Comment on the morphology of the red blood cells.
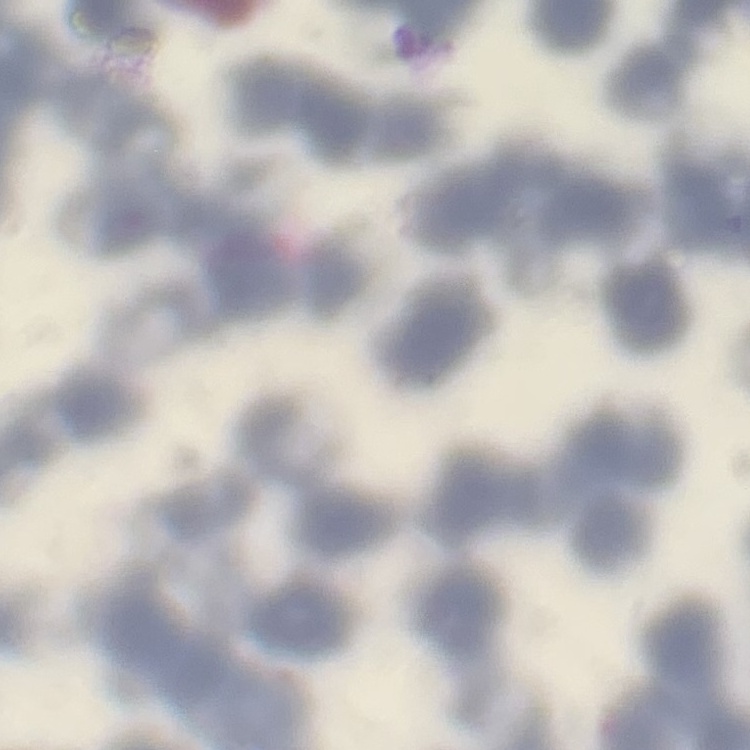

Rouleaux formation.

Summary:
  - Image type: one tile cut from a larger photomicrograph
  - Preparation: thin blood film
  - Stain: Field's or Giemsa